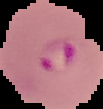
malaria status = parasitized
image size = 103×109 pixels
preparation = thin blood film
image type = segmented cell region with the area outside set to black